Assess this cell for malaria.
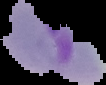

Parasitized.

From a thin blood film. Cell region segmented out of the field of view; the surrounding area is masked to black. Image is 106×85 pixels.